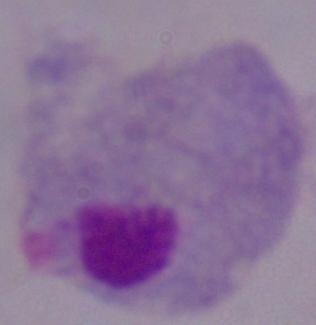

A trichomonad is shown. Captured at 1000x magnification. Micrograph.